Evaluate for malaria.
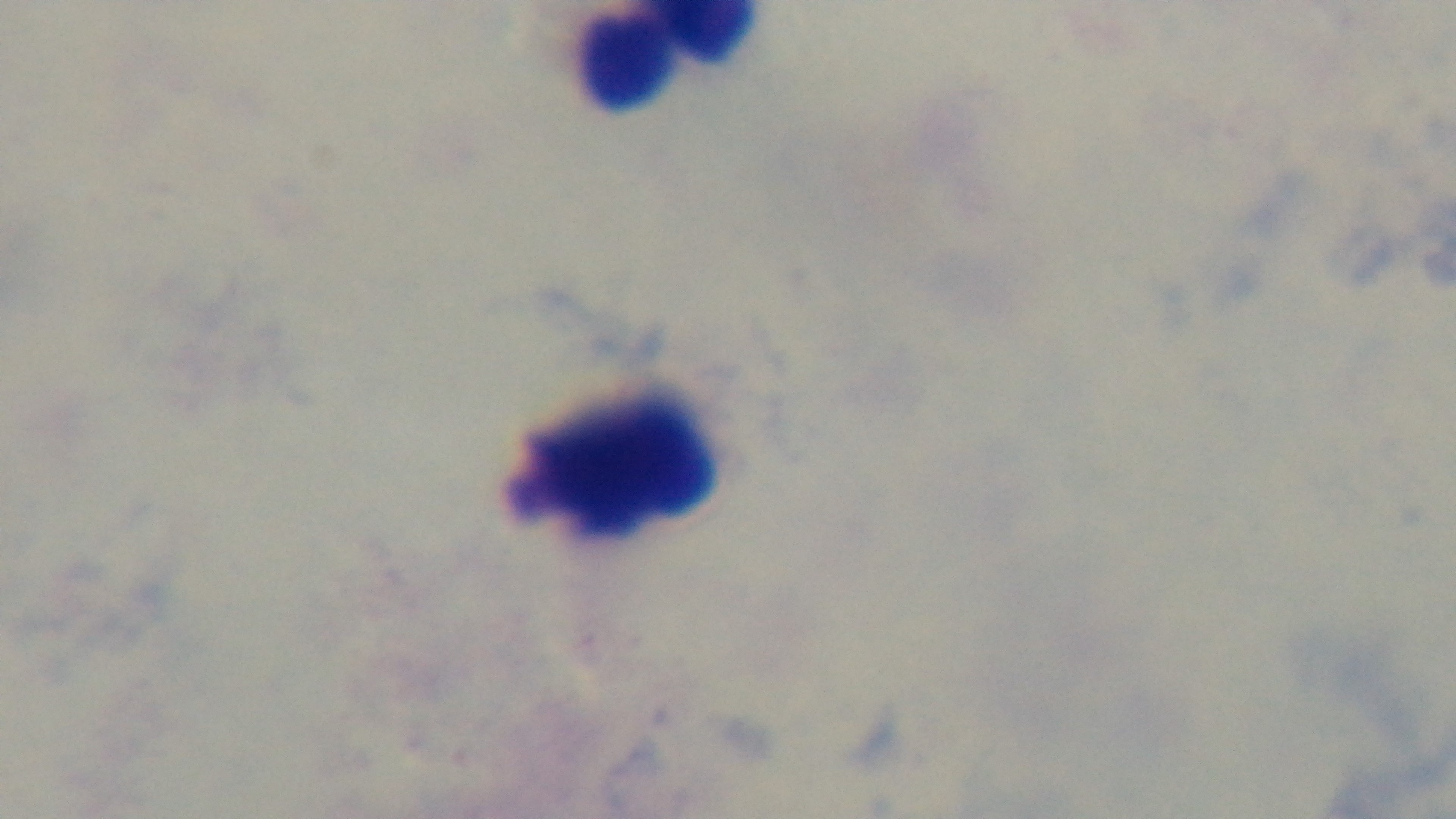

It is uninfected.

objective = 100x oil immersion
field of view = single
preparation = thick blood film
stain = Giemsa
capture = mounted 4K digital camera
modality = light microscopy